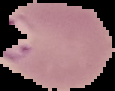
{
  "image_size": "115×91 pixels",
  "preparation": "thin blood film",
  "image_type": "segmented cell region on a black background",
  "result": "malaria parasites detected"
}